Classify this cell by malaria status.
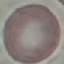
Uninfected.

Automatically extracted cell patch, resized to 64 × 64 pixels. Giemsa-stained preparation. Thin blood film. Acquired by smartphone through the microscope eyepiece.